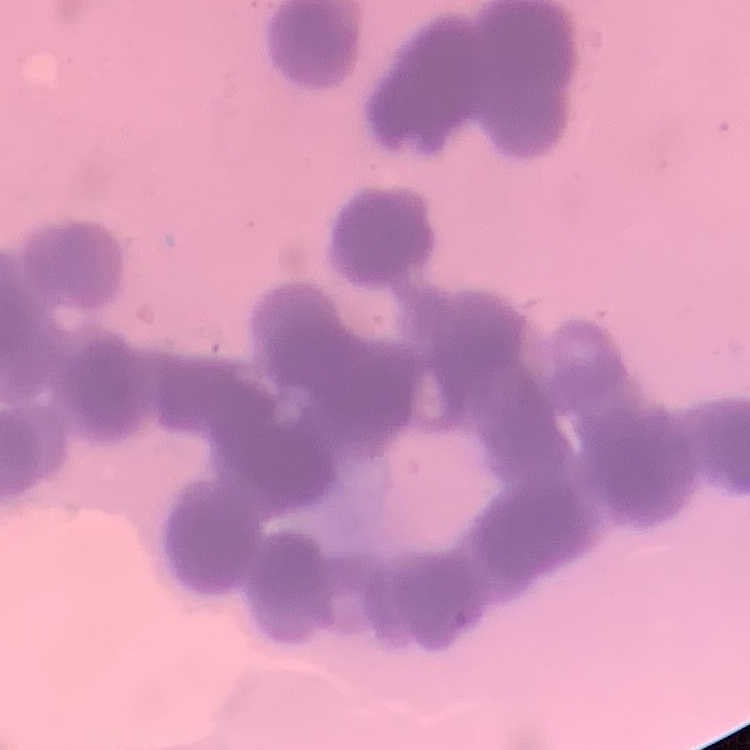
The erythrocytes exhibit rouleaux formation. Thin blood film. Square crop of a larger photomicrograph. Stained with either Field's or Giemsa.